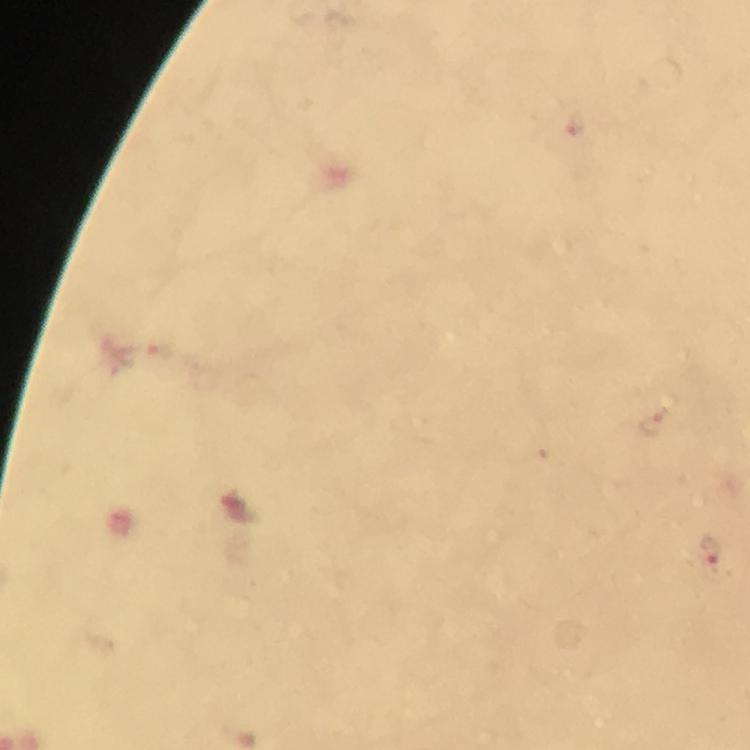

Approximate centers as [x, y] in pixels.
Summary:
  - Malaria parasite locations: [651, 422], [712, 555]
  - Stain: Giemsa
  - Magnification: 100x
  - Preparation: thick blood smear
  - Cropped from: a single field of view
  - Image size: 750×750 pixels
  - Capture: smartphone photograph through a microscope
  - Context: from a diagnostic examination for malaria
  - Immersion oil: used